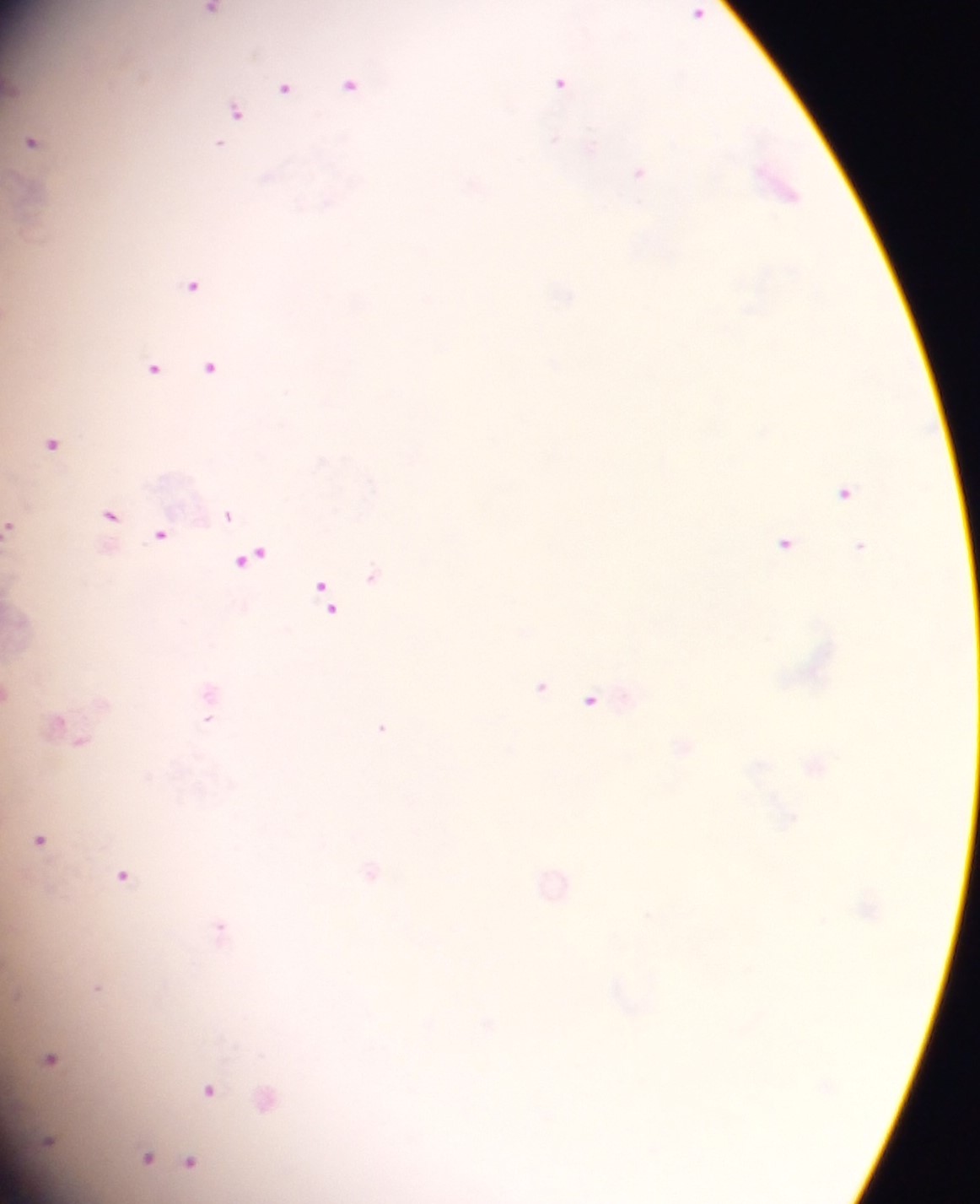
Approximate centers as x y in pixels. Plasmodium parasite locations: 211 10; 698 13; 562 82; 351 85; 284 86; 236 112; 32 141; 219 146; 639 172; 778 184; 193 284; 209 366; 154 367; 52 444; 846 492; 111 514; 228 515; 11 526; 161 535; 785 542; 860 546; 252 555; 373 576; 327 601; 540 687; 9 692; 209 695; 591 700; 208 709; 381 727; 68 732; 815 764; 39 839; 371 871; 123 875; 554 881; 221 928; 97 988; 50 1058; 209 1089; 267 1097; 49 1141; 147 1156; 166 1159; 190 1161. Collected in Ghana. One field of view. Thick blood film. Image is 980×1204 pixels. Mobile-phone photograph taken through the microscope.